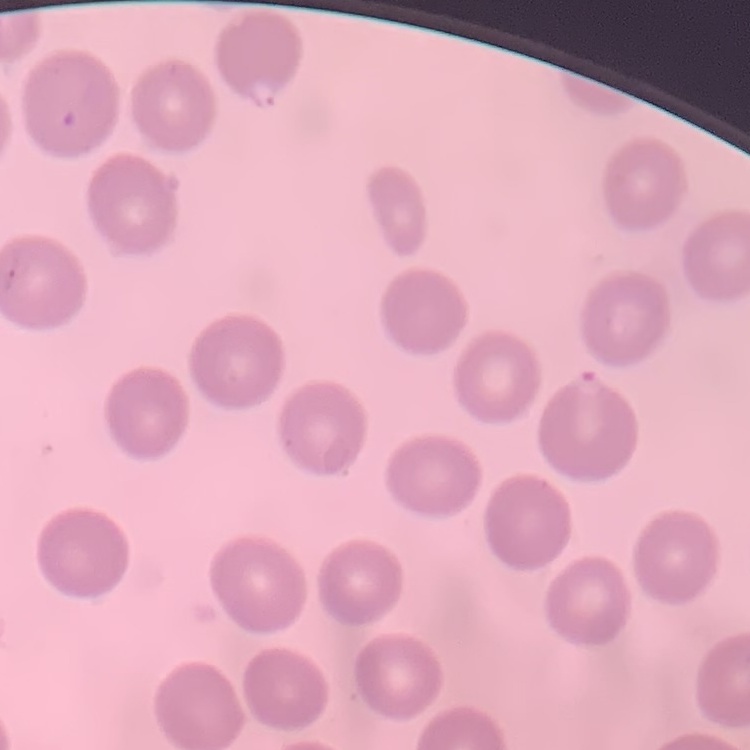

The red blood cells show no rouleaux formation. One tile cut from a larger photomicrograph. Thin blood smear. Field's or Giemsa stain.